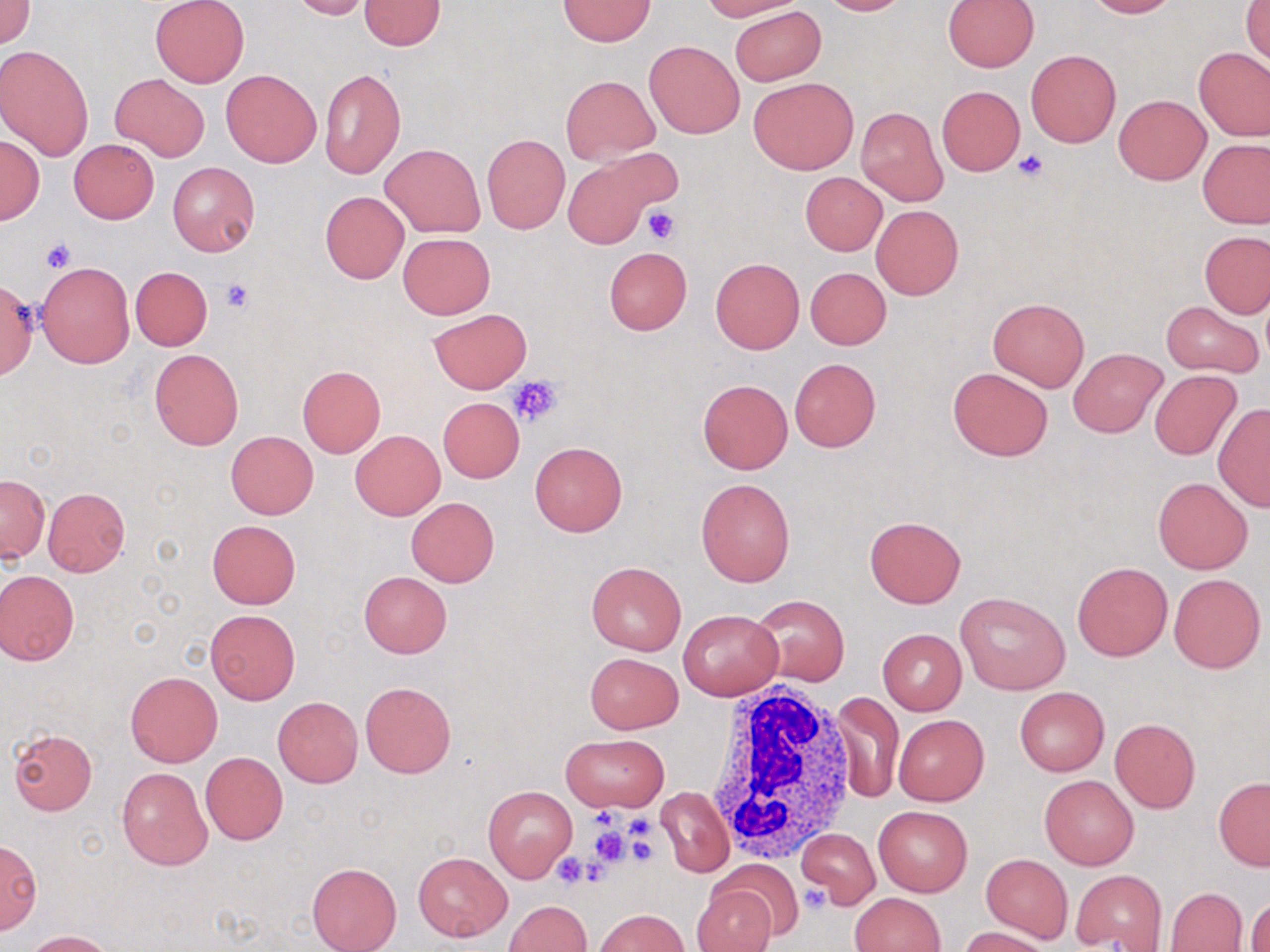
slide_level_diagnosis: negative for blood parasites
stain: May-Grünwald-Giemsa
white_blood_cell_locations: 'approximate bounding boxes as (x1,y1)-(x2,y2) corner pairs in pixels: (699,688)-(860,862)'
magnification: 1000x
modality: optical microscopy
image_size: 1270×952 pixels
field_of_view: single
preparation: thin blood film
platelet_locations: 'approximate bounding boxes as (x1,y1)-(x2,y2) corner pairs in pixels: (1013,149)-(1049,181), (643,205)-(680,244), (42,239)-(77,274), (219,279)-(254,314), (17,297)-(49,336), (509,375)-(563,427), (593,807)-(616,830), (630,816)-(656,837), (586,825)-(635,869), (622,832)-(660,867), (551,852)-(591,888), (798,884)-(831,915)'
uninfected_red_blood_cell_locations: 'approximate bounding boxes as (x1,y1)-(x2,y2) corner pairs in pixels: (1,0)-(35,48), (150,0)-(249,87), (287,0)-(371,20), (700,0)-(806,20), (817,0)-(909,15), (1084,0)-(1180,18), (357,1)-(446,49), (559,1)-(656,45), (943,1)-(1040,73), (1242,2)-(1270,65), (731,6)-(826,85), (643,40)-(745,139), (0,44)-(96,160), (1194,48)-(1270,141), (1026,49)-(1121,147), (318,68)-(405,179), (221,69)-(322,167), (110,73)-(209,162), (561,75)-(659,164), (748,77)-(858,174), (936,84)-(1026,177), (1114,95)-(1210,184), (856,106)-(947,206), (482,134)-(571,235), (0,136)-(43,224), (68,139)-(159,224), (1197,139)-(1269,228), (381,144)-(485,237), (167,162)-(260,257), (563,162)-(655,248), (800,172)-(887,256), (320,191)-(409,283), (870,204)-(964,300), (1199,231)-(1269,318), (399,233)-(494,318), (603,246)-(692,334), (710,256)-(805,354), (37,262)-(134,367), (130,266)-(212,350), (805,266)-(890,350), (1,280)-(38,378), (986,297)-(1090,391), (1159,300)-(1263,379), (429,308)-(532,393), (1069,346)-(1168,438), (149,349)-(243,449), (789,357)-(881,452), (296,365)-(385,459), (947,366)-(1052,460), (1149,369)-(1242,460), (698,378)-(793,473), (437,397)-(524,482), (1212,403)-(1270,510), (351,430)-(445,519), (226,431)-(318,519), (528,442)-(628,536), (1,475)-(50,562), (1153,477)-(1252,574), (695,478)-(795,587), (43,487)-(129,577), (405,497)-(500,588), (863,514)-(966,608), (207,520)-(301,609), (586,560)-(686,656), (1071,560)-(1172,661), (0,569)-(80,666), (359,571)-(451,658), (1168,573)-(1265,673), (955,592)-(1070,694), (750,593)-(850,686), (204,609)-(300,704), (678,609)-(782,700), (878,628)-(966,715), (583,652)-(683,734), (125,670)-(223,767), (359,681)-(457,778), (1014,686)-(1109,775), (831,693)-(904,806), (273,697)-(362,786), (893,715)-(988,806), (1110,718)-(1201,812), (8,728)-(97,816), (562,733)-(669,811), (200,752)-(287,845), (117,768)-(212,870), (1039,775)-(1139,870), (1213,778)-(1270,870), (482,784)-(578,882), (658,786)-(733,877), (874,806)-(972,896), (796,826)-(880,909), (1,837)-(42,935), (414,851)-(512,941), (981,853)-(1072,944), (714,859)-(804,941), (306,862)-(401,952), (1071,869)-(1166,950), (693,886)-(775,952), (1165,887)-(1248,951), (850,892)-(946,952), (1247,897)-(1270,952), (504,901)-(592,952), (594,909)-(689,952), (960,926)-(1053,952), (24,930)-(114,952)'